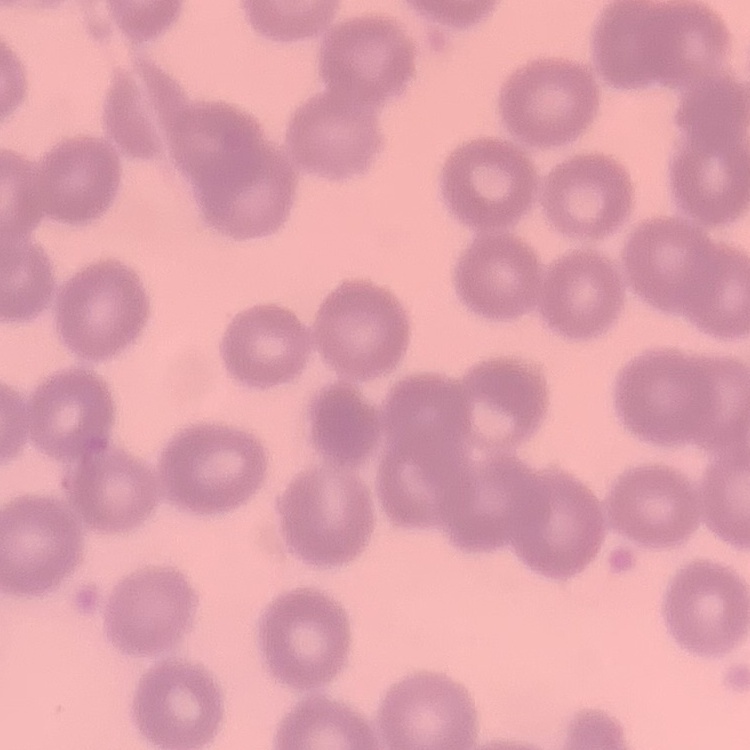
The erythrocytes show no rouleaux formation. Thin blood film. One tile cut from a larger photomicrograph. Stained with either Field's or Giemsa.